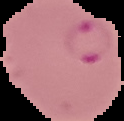
image size = 124×121 pixels
image type = segmented cell region on a black background
preparation = thin blood smear
malaria status = parasitized